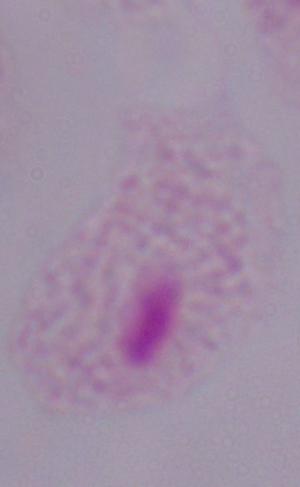

magnification = 1000x
identification = trichomonad
modality = photomicrograph